Locate every Plasmodium parasite and every leukocyte.
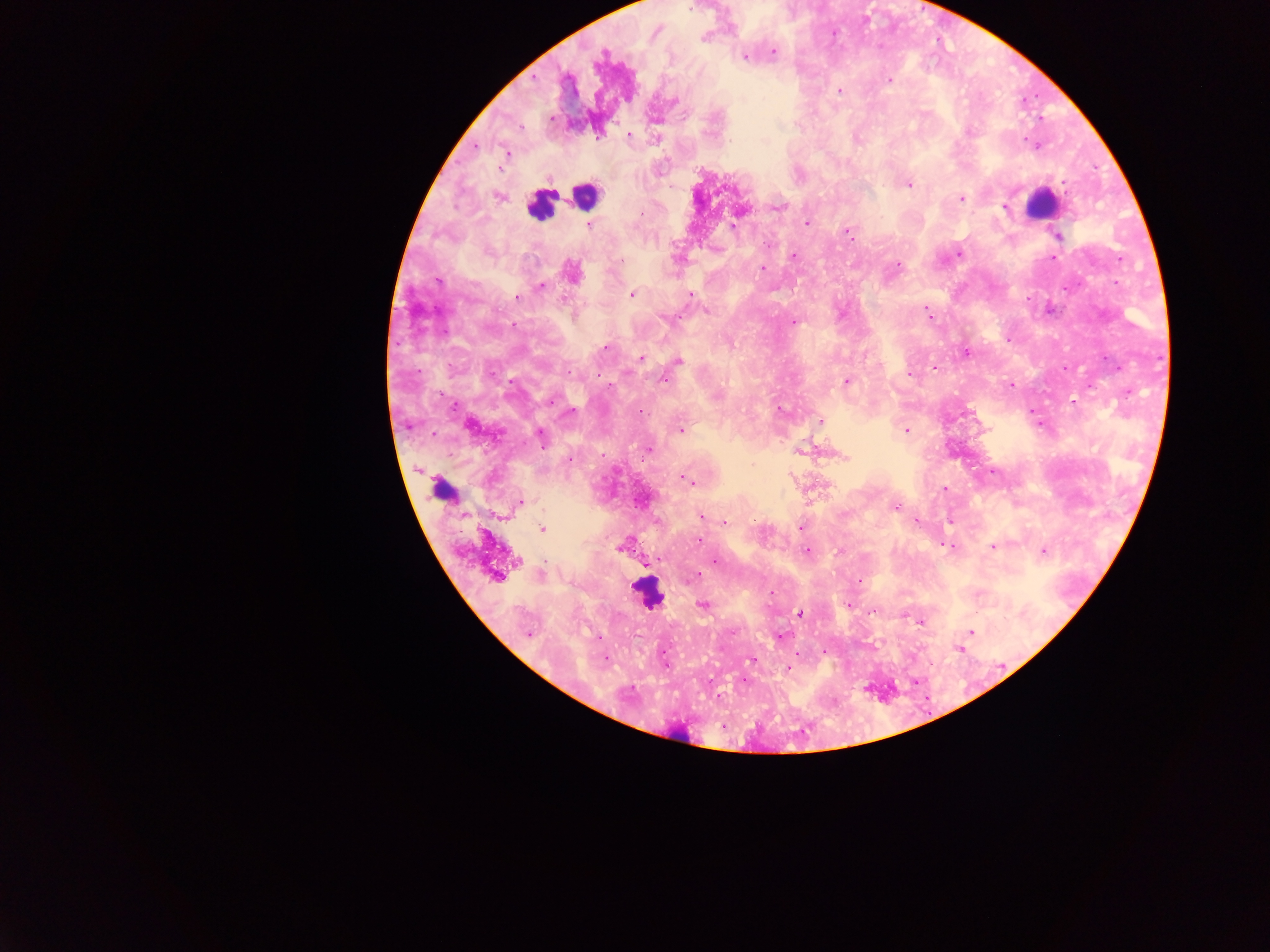
Approximate centers as [x, y] in pixels.
Plasmodium parasites: [703, 38], [773, 52], [604, 53], [745, 57], [889, 80], [839, 90], [551, 118], [520, 127], [598, 135], [630, 135], [506, 153], [908, 184], [498, 197], [961, 198], [1004, 206], [776, 207], [640, 215], [807, 223], [588, 224], [734, 227], [848, 232], [1058, 236], [768, 245], [959, 254], [794, 256], [1054, 257], [899, 264], [762, 268], [571, 272], [541, 285], [632, 294], [690, 295], [517, 297], [706, 311], [927, 312], [666, 319], [793, 322], [606, 347], [966, 352], [641, 358], [679, 360], [934, 368], [491, 373], [908, 374], [664, 380], [846, 381], [1012, 384], [552, 400], [1073, 403], [781, 410], [569, 413], [819, 422], [470, 426], [681, 430], [906, 430], [540, 437], [647, 450], [800, 452], [842, 457], [569, 459], [685, 480], [944, 489], [524, 501], [896, 507], [701, 516], [917, 522], [726, 523], [801, 527], [542, 528], [699, 540], [945, 545], [993, 546], [622, 547], [807, 551], [840, 551], [1043, 552], [656, 560], [715, 561], [651, 562], [497, 575], [695, 576], [859, 580], [848, 604], [703, 605], [801, 614], [921, 622], [971, 632], [528, 634], [780, 636], [959, 650], [605, 658], [752, 660], [788, 668], [744, 681].
Leukocytes: [585, 195], [1039, 202], [540, 205], [442, 483], [647, 594].

Image is 1270×952 pixels. Photographed through a microscope with a mobile-phone camera. Sample from Ghana. Thick blood film. One field of view.